Classify this cell by malaria status.
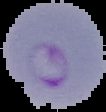
Parasitized.

Segmented cell region on a black background. Image is 106×112 pixels. From a thin blood film.